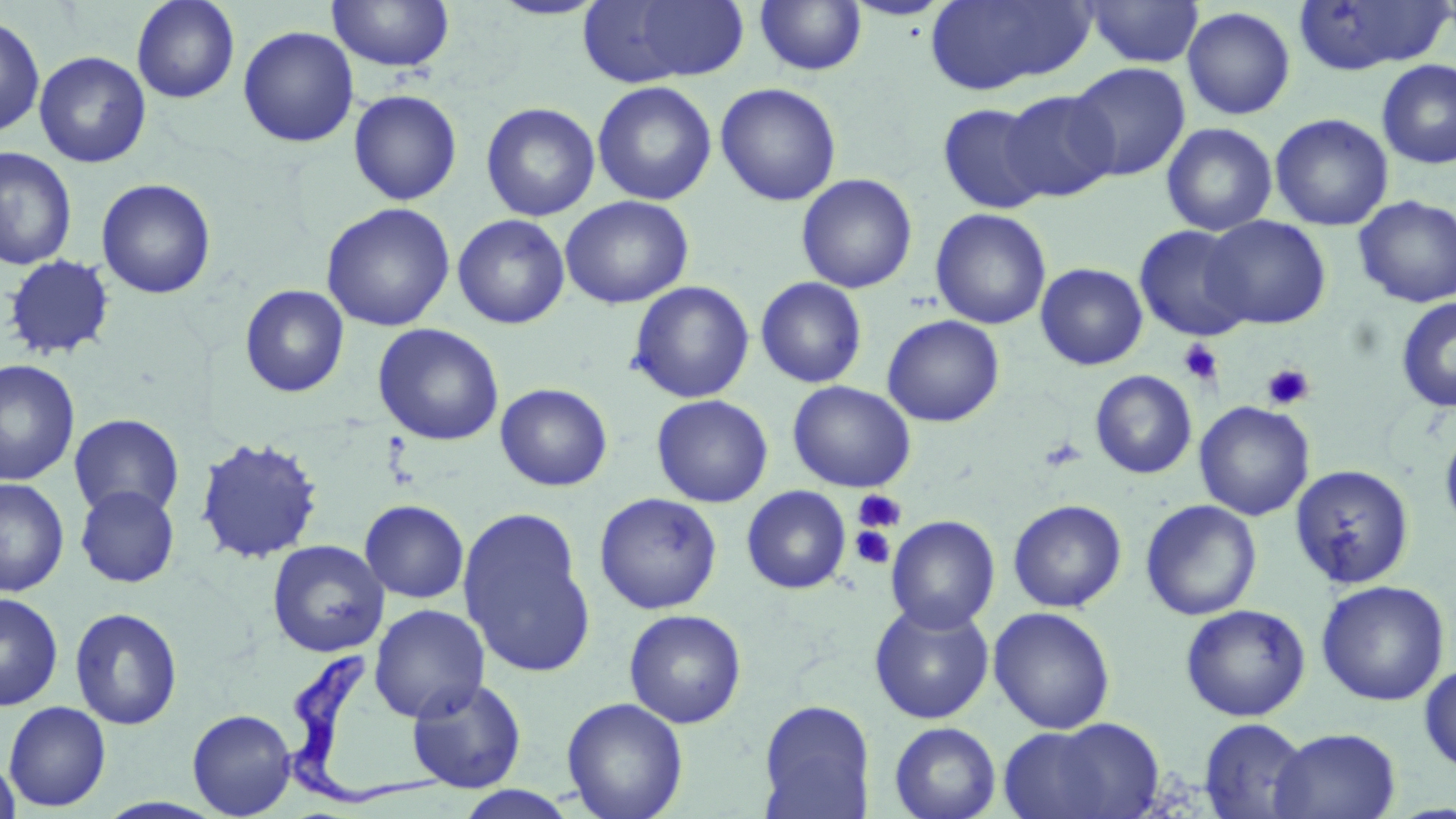
slide-level diagnosis = Trypanosoma brucei
preparation = thin blood film
modality = optical microscopy
magnification = 1000x
platelet locations = approximate bounding boxes as named x1/y1/x2/y2 corners in pixels: (x1=1178, y1=339, x2=1224, y2=386), (x1=1262, y1=363, x2=1316, y2=410), (x1=1039, y1=436, x2=1088, y2=472), (x1=854, y1=488, x2=905, y2=533), (x1=849, y1=525, x2=896, y2=570)
field of view = one of a larger specimen
uninfected red blood cell locations = approximate bounding boxes as named x1/y1/x2/y2 corners in pixels: (x1=131, y1=0, x2=240, y2=104), (x1=487, y1=0, x2=610, y2=21), (x1=580, y1=0, x2=753, y2=85), (x1=754, y1=0, x2=868, y2=77), (x1=844, y1=0, x2=952, y2=21), (x1=924, y1=0, x2=1094, y2=96), (x1=1081, y1=0, x2=1204, y2=68), (x1=326, y1=1, x2=455, y2=73), (x1=1293, y1=1, x2=1451, y2=76), (x1=1182, y1=6, x2=1296, y2=120), (x1=0, y1=13, x2=45, y2=138), (x1=237, y1=25, x2=359, y2=148), (x1=34, y1=51, x2=151, y2=168), (x1=1375, y1=59, x2=1456, y2=169), (x1=1068, y1=63, x2=1190, y2=181), (x1=592, y1=81, x2=717, y2=206), (x1=715, y1=82, x2=841, y2=207), (x1=348, y1=89, x2=462, y2=206), (x1=1000, y1=89, x2=1120, y2=202), (x1=347, y1=93, x2=596, y2=207), (x1=481, y1=102, x2=600, y2=221), (x1=937, y1=103, x2=1050, y2=214), (x1=1270, y1=113, x2=1393, y2=231), (x1=1161, y1=122, x2=1278, y2=236), (x1=0, y1=147, x2=77, y2=271), (x1=796, y1=173, x2=918, y2=293), (x1=96, y1=178, x2=216, y2=299), (x1=560, y1=195, x2=694, y2=309), (x1=1353, y1=195, x2=1456, y2=307), (x1=320, y1=202, x2=455, y2=332), (x1=930, y1=208, x2=1052, y2=330), (x1=452, y1=214, x2=571, y2=329), (x1=1203, y1=215, x2=1331, y2=330), (x1=1134, y1=225, x2=1254, y2=341), (x1=3, y1=254, x2=116, y2=361), (x1=1035, y1=262, x2=1148, y2=370), (x1=755, y1=276, x2=868, y2=389), (x1=627, y1=280, x2=755, y2=404), (x1=240, y1=284, x2=349, y2=398), (x1=1395, y1=296, x2=1456, y2=413), (x1=882, y1=314, x2=1004, y2=427), (x1=372, y1=323, x2=504, y2=446), (x1=0, y1=359, x2=80, y2=487), (x1=1090, y1=370, x2=1197, y2=479), (x1=787, y1=380, x2=916, y2=493), (x1=494, y1=382, x2=613, y2=491), (x1=651, y1=394, x2=773, y2=508), (x1=1194, y1=400, x2=1315, y2=521), (x1=69, y1=413, x2=184, y2=520), (x1=1440, y1=419, x2=1456, y2=539), (x1=194, y1=436, x2=325, y2=565), (x1=1289, y1=464, x2=1415, y2=589), (x1=0, y1=478, x2=70, y2=596), (x1=74, y1=486, x2=179, y2=587), (x1=741, y1=486, x2=851, y2=594), (x1=594, y1=492, x2=723, y2=615), (x1=359, y1=499, x2=470, y2=603), (x1=1008, y1=499, x2=1127, y2=612), (x1=1140, y1=499, x2=1262, y2=620), (x1=458, y1=506, x2=596, y2=679), (x1=886, y1=515, x2=1000, y2=633), (x1=267, y1=539, x2=390, y2=657), (x1=1315, y1=580, x2=1450, y2=706), (x1=0, y1=591, x2=63, y2=711), (x1=869, y1=601, x2=994, y2=724), (x1=369, y1=603, x2=490, y2=723), (x1=1180, y1=603, x2=1311, y2=721), (x1=69, y1=606, x2=183, y2=729), (x1=988, y1=607, x2=1116, y2=733), (x1=624, y1=608, x2=747, y2=729), (x1=1419, y1=663, x2=1456, y2=774), (x1=407, y1=677, x2=527, y2=793), (x1=561, y1=697, x2=689, y2=819), (x1=757, y1=699, x2=875, y2=818), (x1=3, y1=701, x2=111, y2=812), (x1=188, y1=709, x2=297, y2=817), (x1=1004, y1=716, x2=1165, y2=818), (x1=1198, y1=718, x2=1310, y2=818), (x1=888, y1=722, x2=1001, y2=819), (x1=1269, y1=727, x2=1401, y2=819), (x1=0, y1=757, x2=21, y2=819), (x1=449, y1=785, x2=582, y2=818)
stain = May-Grünwald-Giemsa
Trypanosoma brucei locations = approximate bounding boxes as named x1/y1/x2/y2 corners in pixels: (x1=274, y1=650, x2=446, y2=802)
image size = 1456×819 pixels